Assess the morphology of the red blood cells.
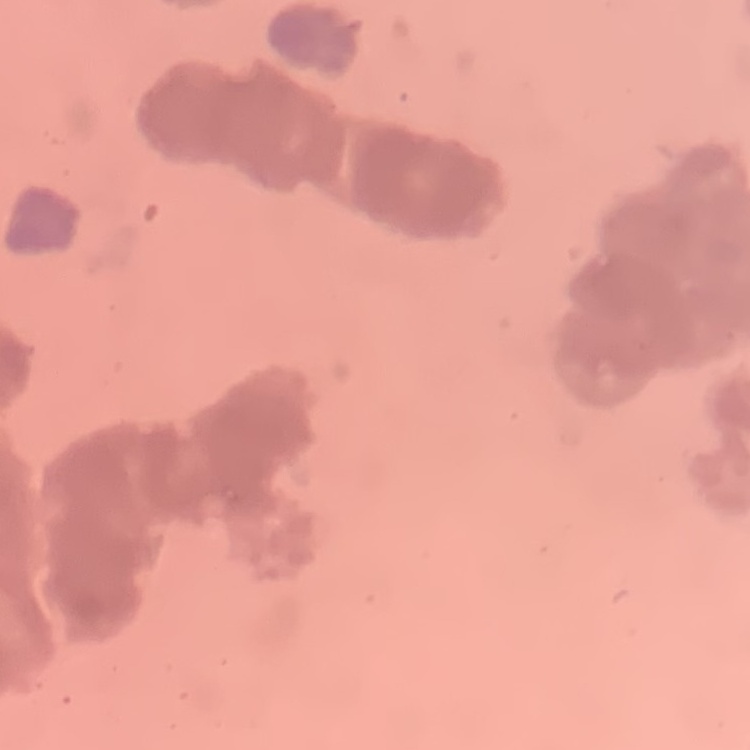

Rouleaux formation.

Summary:
  - Preparation: thin blood film
  - Stain: Field's or Giemsa
  - Image type: one tile cut from a larger photomicrograph